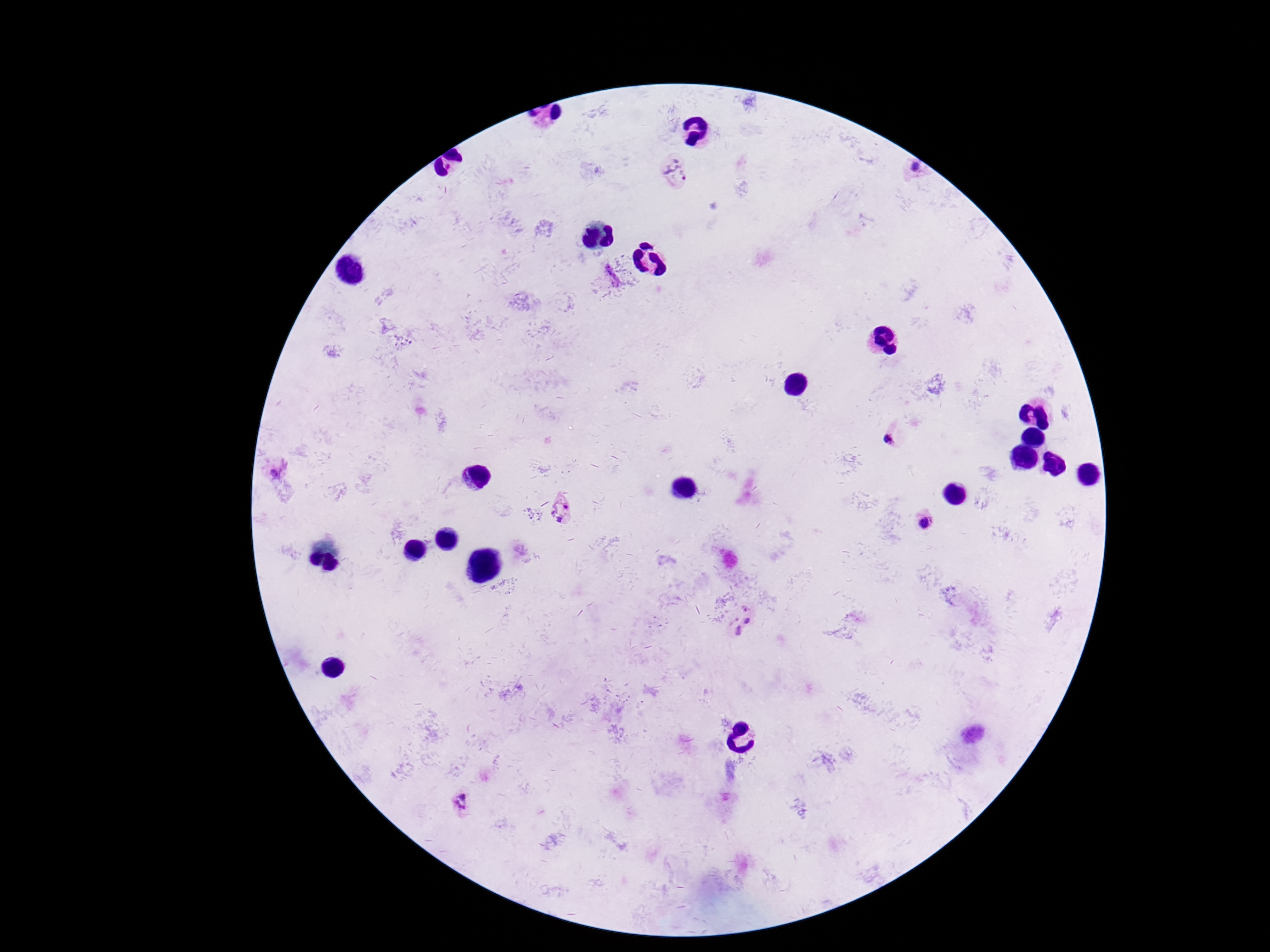
patient malaria status = positive
magnification = 100x
capture = smartphone camera through the microscope eyepiece
image size = 1270×952 pixels
preparation = thick blood film
Plasmodium parasite locations = approximate centers as [x, y] in pixels: [913, 170], [675, 174], [611, 276], [890, 440], [562, 510], [927, 522], [746, 624], [462, 804]
stain = Giemsa
field of view = one from this slide